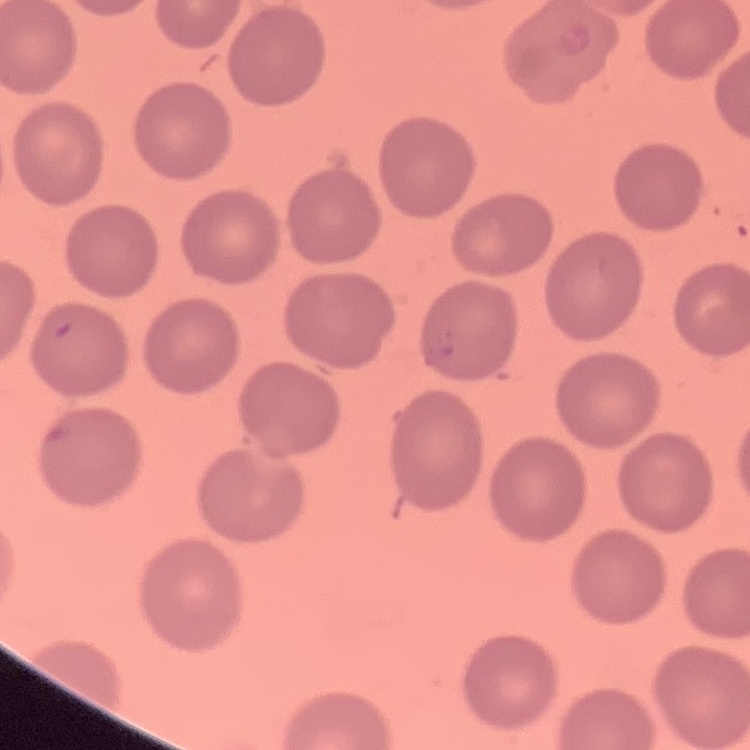

Summary:
  - Erythrocyte morphology: no rouleaux formation
  - Image type: one tile cut from a larger photomicrograph
  - Stain: Field's or Giemsa
  - Preparation: thin blood smear